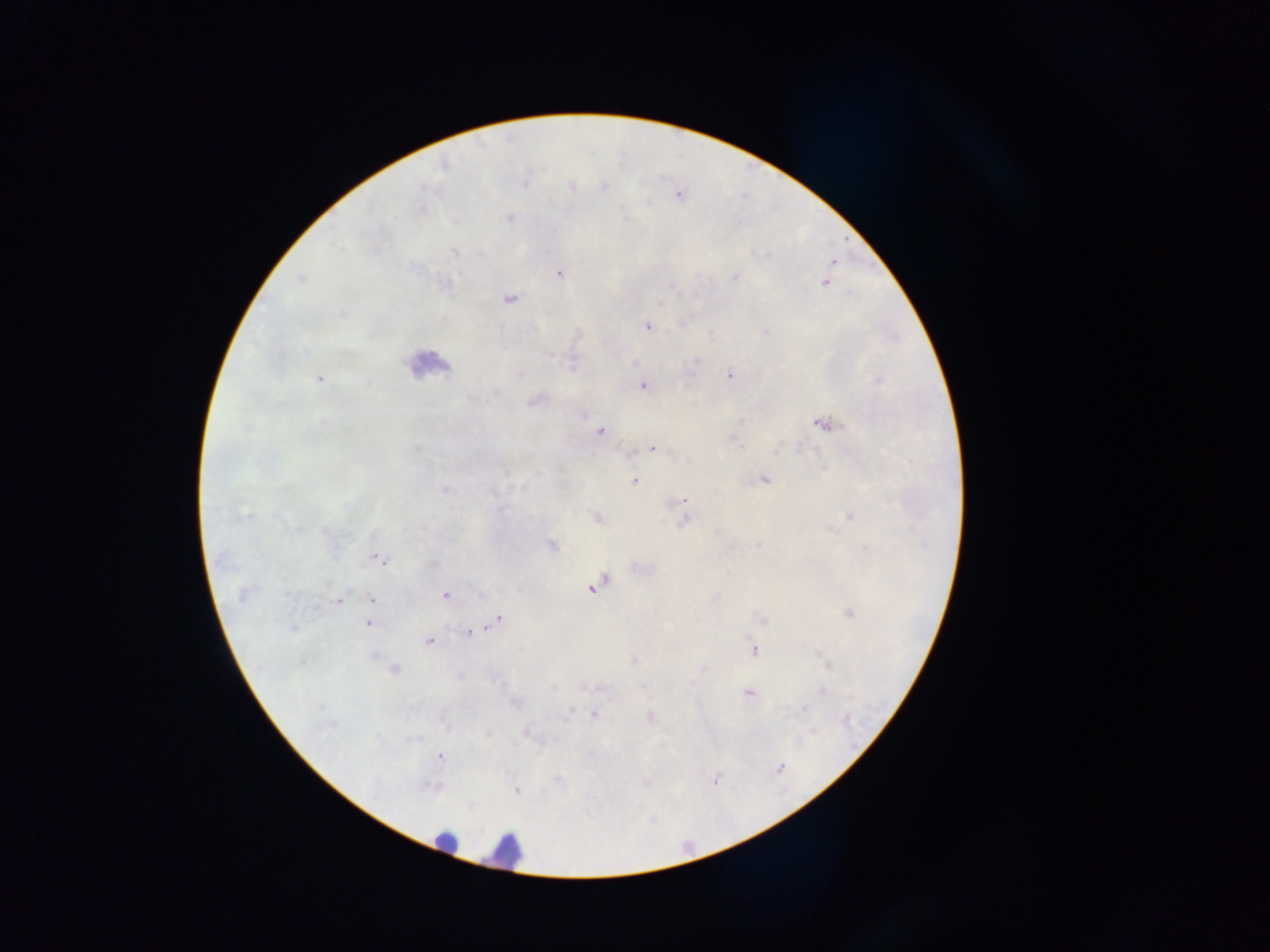
preparation = thick blood smear
field of view = single
leukocyte locations = approximate centers as [x, y] in pixels: [423, 360], [438, 835], [505, 853]
image size = 1270×952 pixels
country = Ghana
capture = mobile-phone photograph through a microscope
Plasmodium parasite locations = approximate centers as [x, y] in pixels: [832, 264], [561, 274], [300, 278], [825, 283], [511, 298], [341, 313], [646, 327], [729, 374], [320, 379], [642, 387], [827, 420], [600, 433], [654, 448], [634, 481], [685, 501], [374, 557], [381, 561], [593, 587], [445, 595], [372, 599], [337, 600], [498, 620], [369, 624], [484, 630], [469, 633], [429, 641], [754, 651], [748, 693], [804, 710], [440, 757], [781, 768], [714, 779], [517, 790]